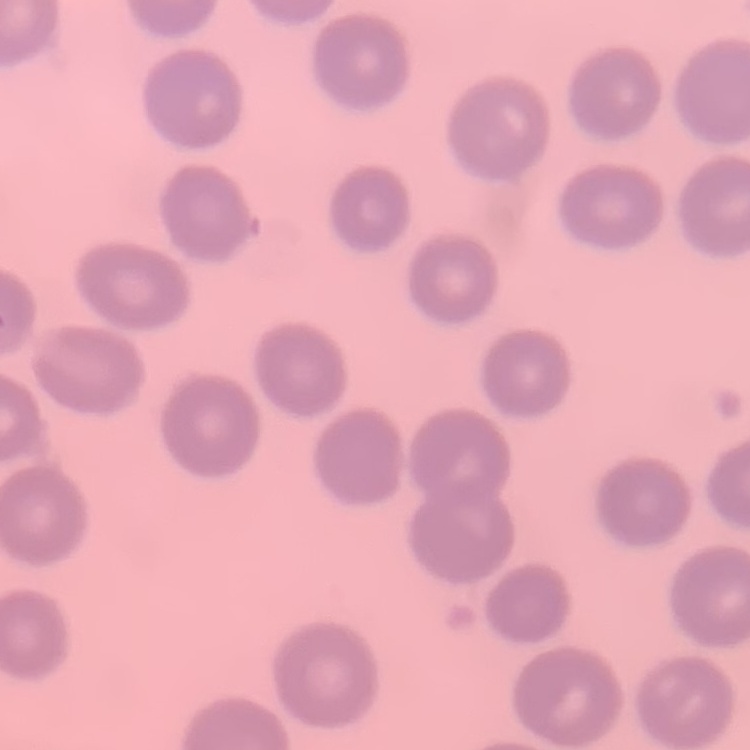

{
  "red_blood_cell_morphology": "no rouleaux formation",
  "preparation": "thin blood film",
  "image_type": "one tile cut from a larger photomicrograph",
  "stain": "Field's or Giemsa"
}